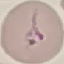

Summary:
  - Result: negative for malaria parasites
  - Preparation: thin blood smear
  - Stain: Giemsa
  - Capture: smartphone camera at the microscope eyepiece
  - Image type: cell patch, automatically extracted from a larger field of view and resized to 64 × 64 pixels